Locate and identify every blood parasite.
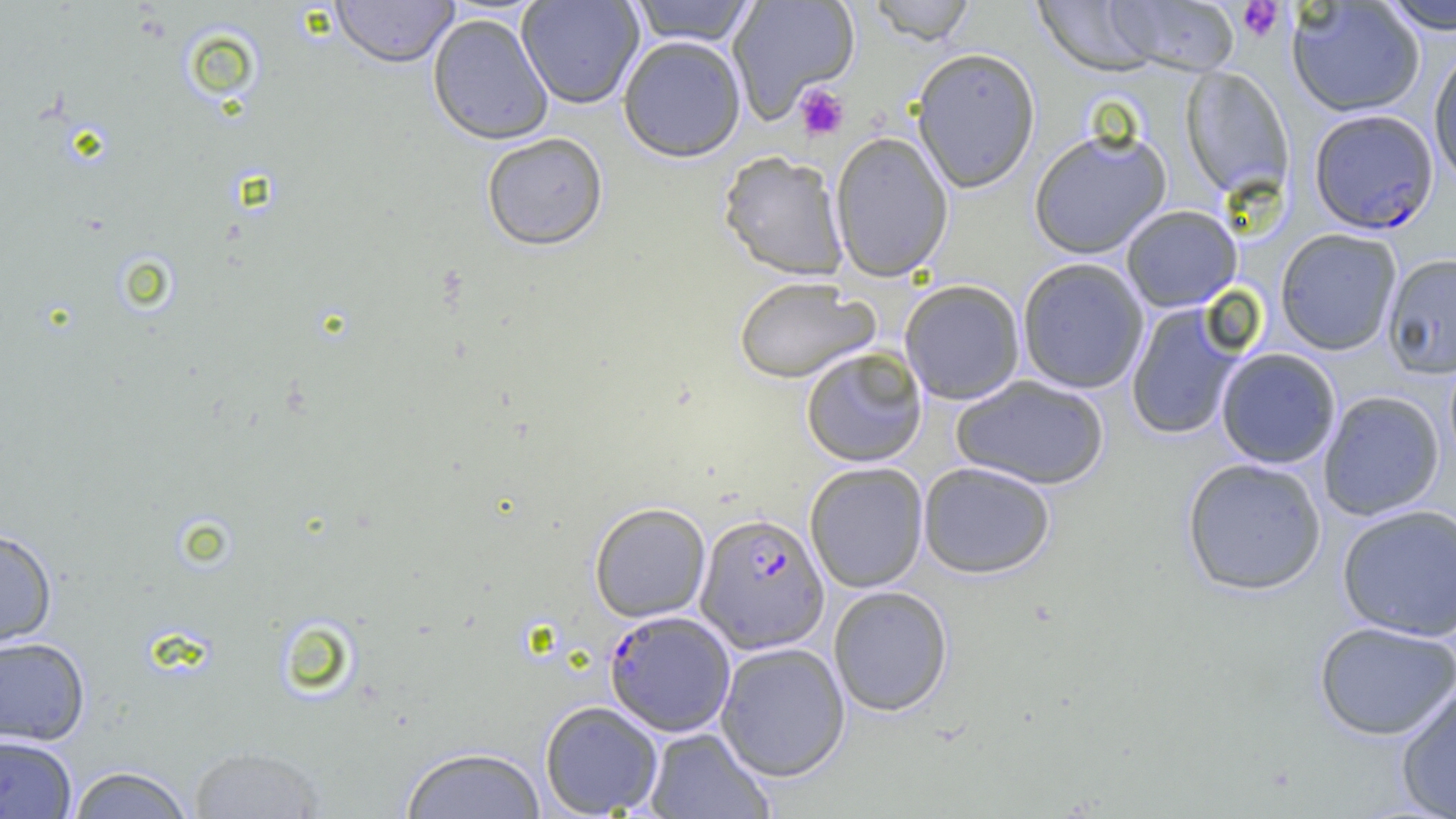

Approximate bounding boxes as named x1/y1/x2/y2 corners in pixels.
Plasmodium falciparum-infected red blood cells (subset): (x1=695, y1=512, x2=829, y2=653), (x1=604, y1=609, x2=735, y2=737).
No Plasmodium ovale, Plasmodium malariae, Plasmodium vivax, Babesia divergens, or Trypanosoma brucei observed.

slide-level diagnosis = Plasmodium falciparum
modality = optical microscopy
magnification = 1000x
preparation = thin blood film
image size = 1456×819 pixels
uninfected red blood cell locations (subset) = approximate bounding boxes as named x1/y1/x2/y2 corners in pixels: (x1=331, y1=0, x2=459, y2=69), (x1=517, y1=0, x2=644, y2=109), (x1=628, y1=0, x2=759, y2=47), (x1=727, y1=0, x2=860, y2=121), (x1=866, y1=0, x2=977, y2=45), (x1=1105, y1=0, x2=1241, y2=76), (x1=1031, y1=1, x2=1165, y2=76), (x1=1287, y1=1, x2=1425, y2=117), (x1=1378, y1=1, x2=1456, y2=34), (x1=427, y1=14, x2=554, y2=145), (x1=617, y1=35, x2=747, y2=162), (x1=1428, y1=45, x2=1455, y2=187), (x1=911, y1=47, x2=1041, y2=193), (x1=1180, y1=66, x2=1293, y2=199), (x1=1028, y1=127, x2=1172, y2=259), (x1=829, y1=131, x2=953, y2=282), (x1=481, y1=132, x2=609, y2=251), (x1=718, y1=150, x2=849, y2=281), (x1=1121, y1=205, x2=1243, y2=312), (x1=1275, y1=228, x2=1403, y2=355), (x1=1382, y1=253, x2=1456, y2=378), (x1=1016, y1=258, x2=1150, y2=394), (x1=733, y1=277, x2=879, y2=384), (x1=898, y1=279, x2=1026, y2=405), (x1=1125, y1=302, x2=1246, y2=441), (x1=801, y1=347, x2=928, y2=467), (x1=1215, y1=348, x2=1341, y2=469), (x1=951, y1=375, x2=1110, y2=490), (x1=1318, y1=390, x2=1445, y2=521), (x1=1181, y1=457, x2=1327, y2=596), (x1=918, y1=461, x2=1056, y2=579), (x1=804, y1=462, x2=929, y2=593), (x1=589, y1=502, x2=711, y2=623), (x1=1336, y1=504, x2=1456, y2=641), (x1=0, y1=527, x2=58, y2=651), (x1=828, y1=585, x2=953, y2=716), (x1=1314, y1=620, x2=1456, y2=741), (x1=0, y1=636, x2=90, y2=747), (x1=715, y1=642, x2=851, y2=782), (x1=1395, y1=680, x2=1456, y2=818), (x1=539, y1=700, x2=663, y2=817), (x1=644, y1=727, x2=776, y2=819), (x1=0, y1=734, x2=78, y2=818), (x1=187, y1=745, x2=327, y2=818), (x1=400, y1=746, x2=546, y2=818), (x1=66, y1=765, x2=196, y2=818)
field of view = one of a larger specimen
platelet locations = approximate bounding boxes as named x1/y1/x2/y2 corners in pixels: (x1=1236, y1=1, x2=1285, y2=42), (x1=794, y1=83, x2=850, y2=141)